Name the blood parasite species.
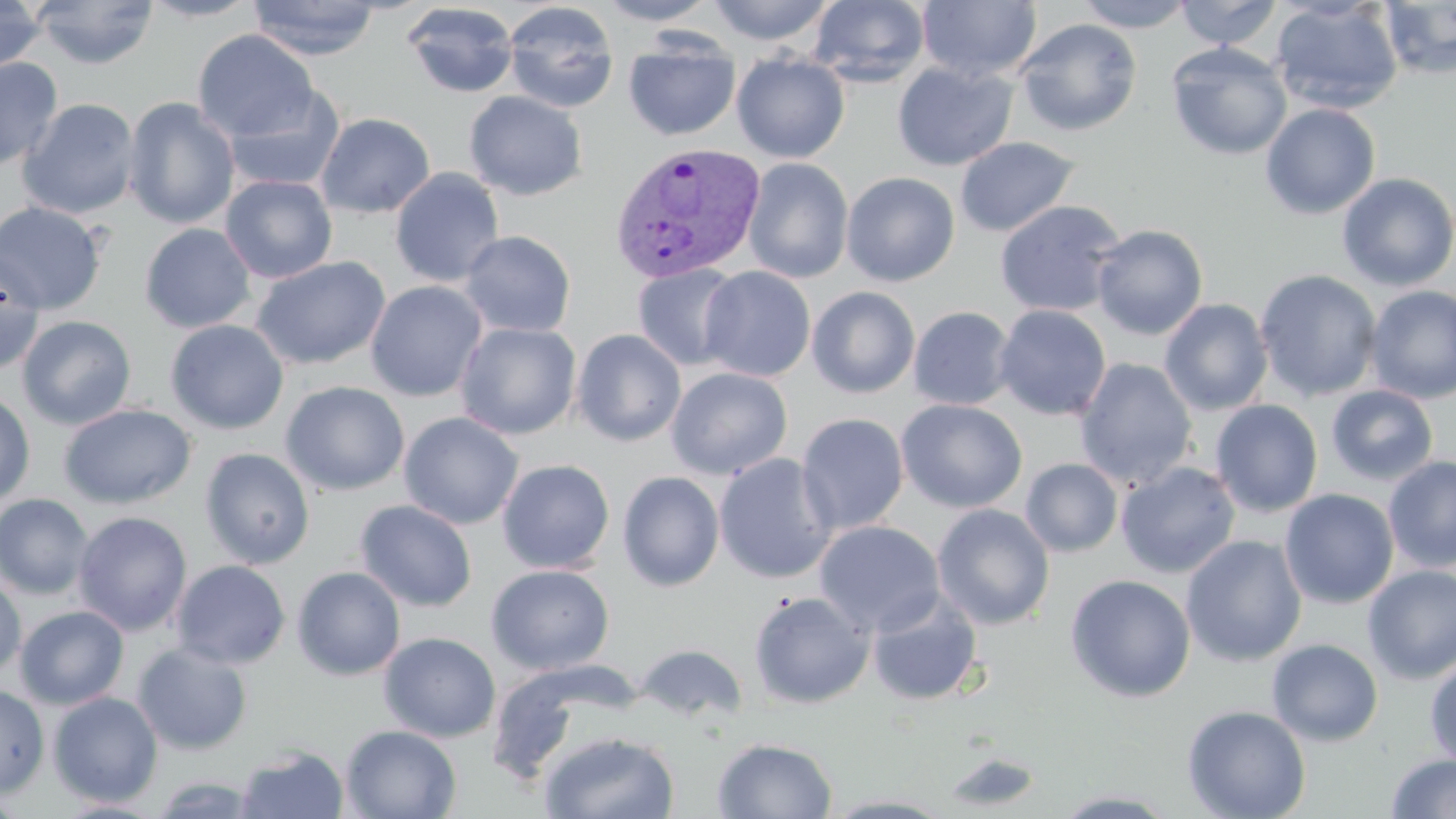
Plasmodium vivax.

Summary:
  - Coordinate format: approximate bounding boxes as (x1,y1)-(x2,y2) corner pairs in pixels
  - Uninfected red blood cell locations: (0,0)-(48,73), (31,0)-(160,69), (139,0)-(262,22), (595,0)-(719,25), (707,0)-(835,46), (915,0)-(1042,83), (1072,0)-(1195,31), (1174,0)-(1283,49), (247,1)-(381,60), (807,1)-(931,87), (1269,1)-(1404,115), (1378,1)-(1456,79), (402,2)-(519,98), (503,2)-(619,113), (1014,18)-(1143,136), (192,29)-(319,143), (624,38)-(740,141), (1166,42)-(1292,160), (731,52)-(850,163), (0,57)-(63,171), (892,61)-(1017,171), (223,84)-(345,192), (464,91)-(588,201), (122,97)-(240,230), (17,98)-(141,219), (1260,103)-(1381,220), (315,112)-(435,218), (955,137)-(1079,237), (743,157)-(853,283), (390,167)-(505,287), (842,172)-(960,286), (1336,172)-(1456,292), (220,175)-(338,283), (995,200)-(1126,317), (0,201)-(107,315), (139,223)-(257,333), (1091,223)-(1208,340), (460,230)-(576,337), (0,249)-(45,376), (251,256)-(391,371), (632,263)-(743,370), (698,266)-(816,382), (1254,269)-(1382,402), (365,280)-(488,402), (1364,285)-(1456,404), (807,286)-(920,398), (1159,298)-(1274,416), (994,305)-(1111,421), (908,306)-(1016,410), (17,315)-(137,430), (165,319)-(289,435), (456,322)-(582,440), (571,329)-(686,446), (1075,358)-(1197,489), (666,367)-(792,480), (281,381)-(409,496), (1325,384)-(1438,486), (0,391)-(35,510), (896,399)-(1028,513), (1210,399)-(1324,517), (59,404)-(196,509), (398,412)-(524,530), (795,414)-(909,535), (200,447)-(315,570), (714,453)-(837,584), (960,456)-(1115,608), (1383,456)-(1456,573), (1020,458)-(1123,557), (497,459)-(615,573), (1116,461)-(1241,578), (617,470)-(725,591), (1279,488)-(1399,609), (0,493)-(94,599), (355,500)-(478,612), (932,504)-(1055,630), (72,511)-(192,636), (813,521)-(945,636), (1181,535)-(1307,667), (171,560)-(291,669), (486,564)-(614,675), (1362,565)-(1456,684), (292,567)-(406,681), (0,573)-(26,679), (1065,574)-(1196,702), (748,590)-(876,709), (866,592)-(983,707), (14,605)-(129,710), (378,632)-(501,743), (1266,638)-(1383,746), (132,643)-(252,755), (635,643)-(748,725), (1425,656)-(1456,768), (0,684)-(50,798), (48,691)-(163,808), (1182,705)-(1311,819), (341,724)-(462,818), (539,730)-(680,818), (712,737)-(838,819), (235,746)-(349,819), (940,750)-(1045,812), (1385,753)-(1456,818), (147,774)-(266,817), (1050,789)-(1182,817), (53,799)-(167,818)
  - Plasmodium vivax-infected red blood cell locations: (608,141)-(766,284)
  - Preparation: thin blood film
  - Image size: 1456×819 pixels
  - Field of view: single
  - Stain: May-Grünwald-Giemsa
  - Magnification: 1000x
  - Modality: light microscopy